Locate and identify every blood parasite.
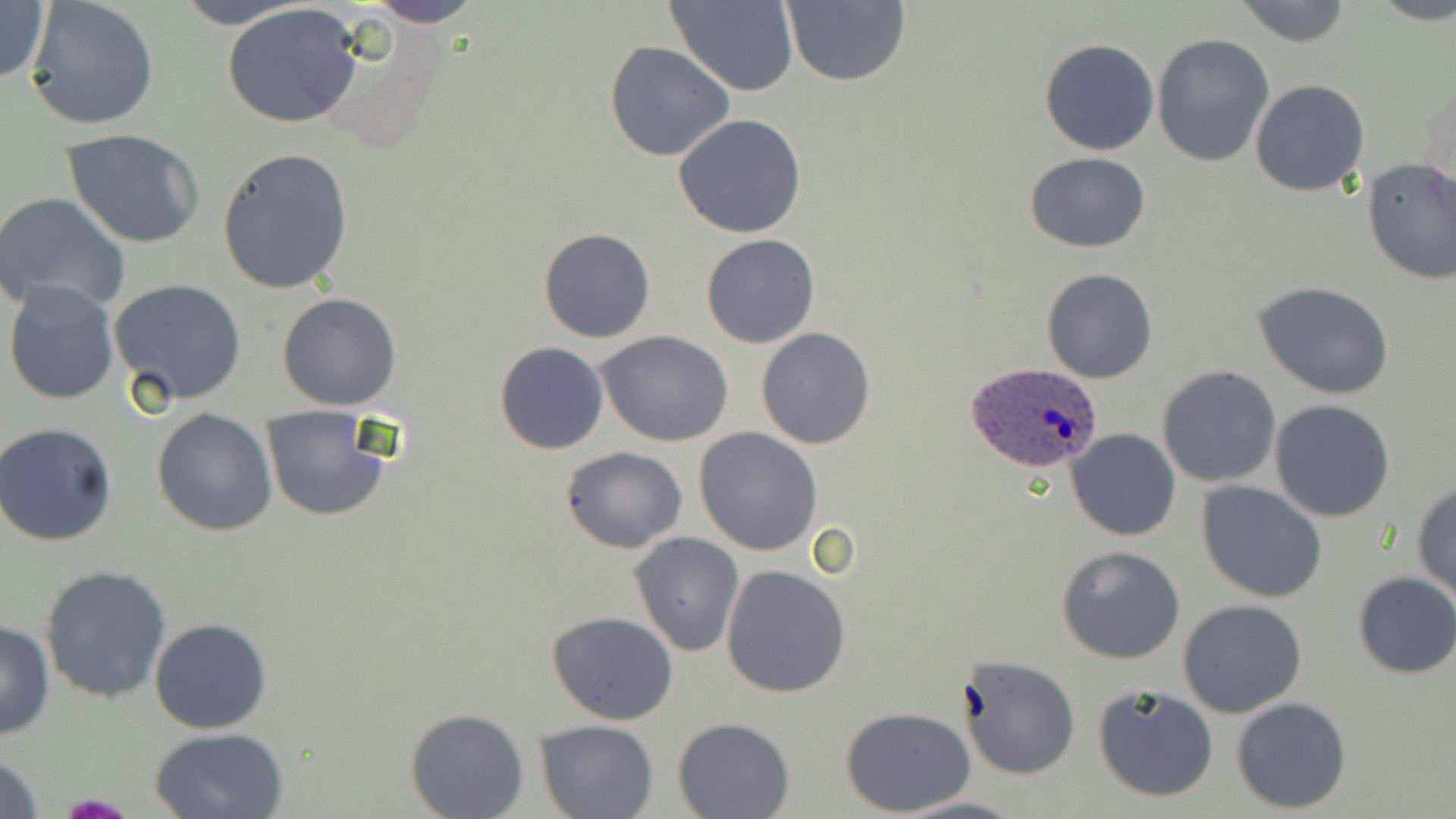
Approximate bounding boxes as (x1, y1, x2, y2) in pixels.
Plasmodium ovale-infected red blood cells: (968, 364, 1103, 474).
No Plasmodium falciparum, Plasmodium malariae, Plasmodium vivax, Babesia divergens, or Trypanosoma brucei observed.

slide-level diagnosis = Plasmodium ovale
uninfected red blood cell locations = approximate bounding boxes as (x1, y1, x2, y2) in pixels: (0, 0, 50, 87), (167, 0, 314, 29), (361, 0, 486, 26), (666, 0, 800, 95), (783, 0, 911, 86), (1231, 0, 1352, 46), (1374, 0, 1456, 26), (222, 2, 365, 128), (26, 3, 158, 130), (1151, 33, 1275, 170), (1040, 38, 1159, 154), (604, 40, 735, 163), (1249, 79, 1370, 198), (674, 114, 807, 239), (61, 127, 206, 248), (216, 146, 354, 295), (1024, 152, 1150, 253), (1360, 158, 1456, 285), (0, 192, 132, 315), (537, 228, 657, 343), (701, 234, 819, 349), (1042, 267, 1158, 384), (109, 279, 249, 407), (4, 280, 121, 406), (1254, 281, 1394, 398), (277, 293, 402, 409), (755, 327, 876, 449), (597, 331, 734, 445), (495, 342, 608, 453), (1157, 364, 1282, 488), (1269, 400, 1396, 522), (260, 404, 390, 523), (151, 407, 277, 536), (1, 422, 119, 545), (693, 428, 824, 556), (1066, 429, 1181, 543), (561, 446, 688, 553), (1412, 478, 1456, 603), (1196, 481, 1327, 604), (629, 531, 746, 659), (1057, 545, 1186, 663), (721, 564, 852, 697), (39, 565, 171, 705), (1351, 571, 1456, 679), (1177, 599, 1308, 719), (547, 611, 678, 726), (0, 617, 55, 740), (149, 618, 273, 735), (959, 654, 1081, 780), (1092, 684, 1219, 802), (1231, 697, 1352, 814), (840, 705, 976, 816), (404, 707, 530, 819), (673, 716, 795, 817), (534, 719, 659, 819), (147, 725, 290, 818), (0, 747, 46, 819), (896, 794, 1027, 818)
modality = light microscopy
image size = 1456×819 pixels
field of view = single
stain = May-Grünwald-Giemsa
magnification = 1000x
preparation = thin blood film